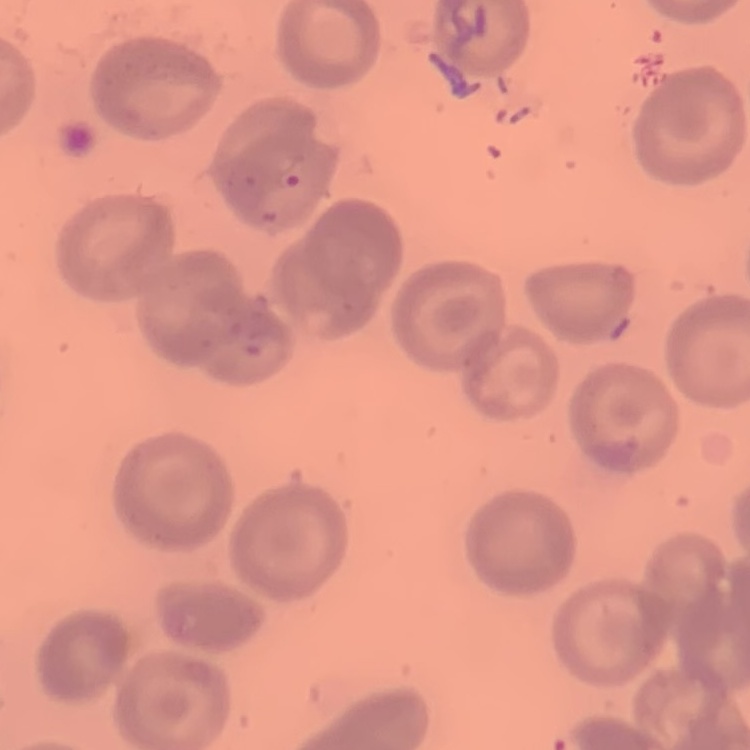 The erythrocytes show no rouleaux formation. One tile cut from a larger photomicrograph. Thin blood film. Field's or Giemsa stain.